Identify the parasite.
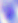
Toxoplasma gondii.

Captured at 400x magnification. Photomicrograph.